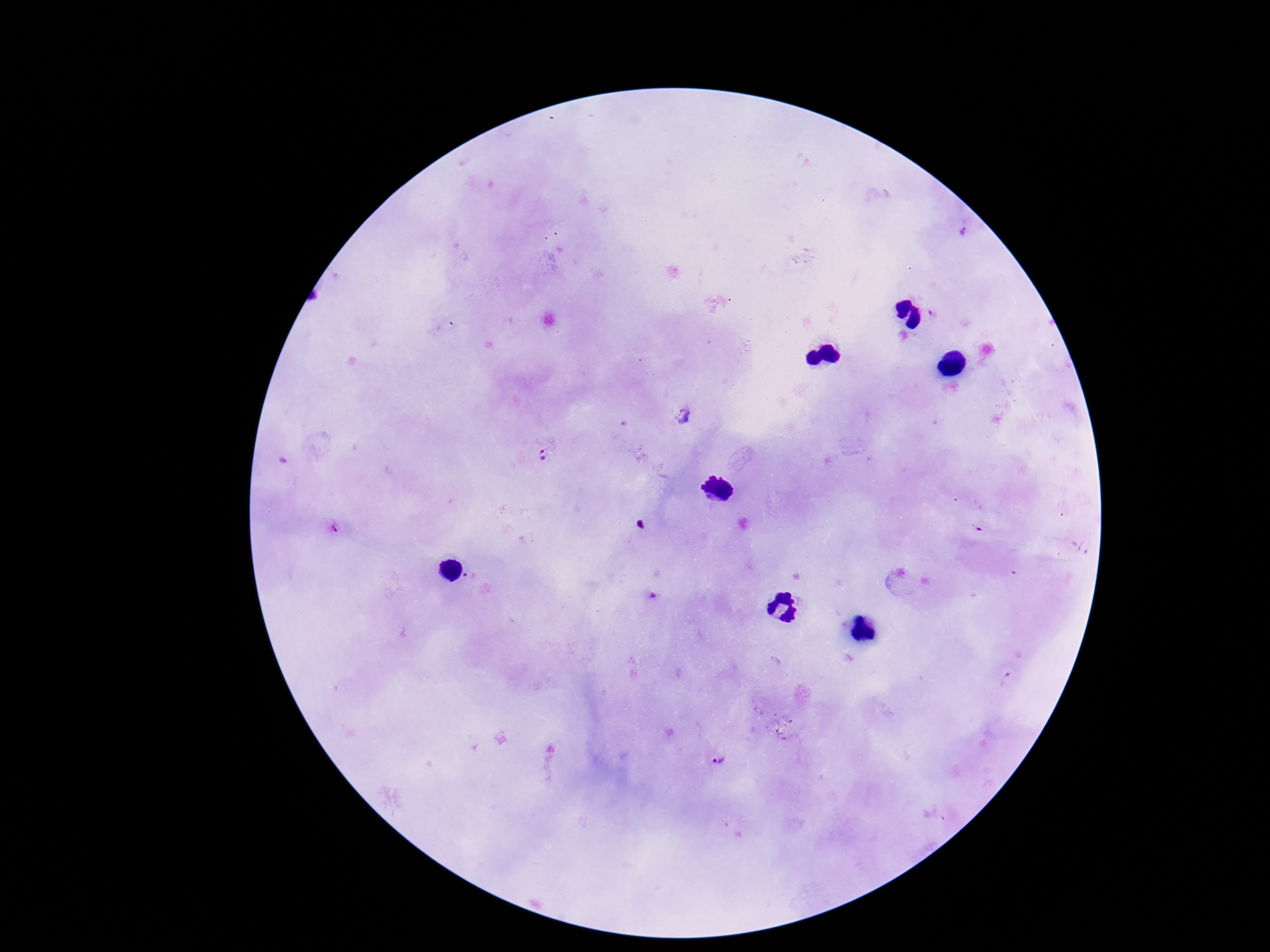

Approximate centers as {x, y} in pixels. Plasmodium parasite locations: {964, 232}, {933, 314}, {684, 415}, {544, 454}, {335, 529}, {469, 577}, {717, 759}. Patient malaria status: positive. 100x magnification. Photographed through the microscope eyepiece with a smartphone camera. Giemsa-stained preparation. Image is 1270×952 pixels. One field from this slide. Thick peripheral-blood smear.